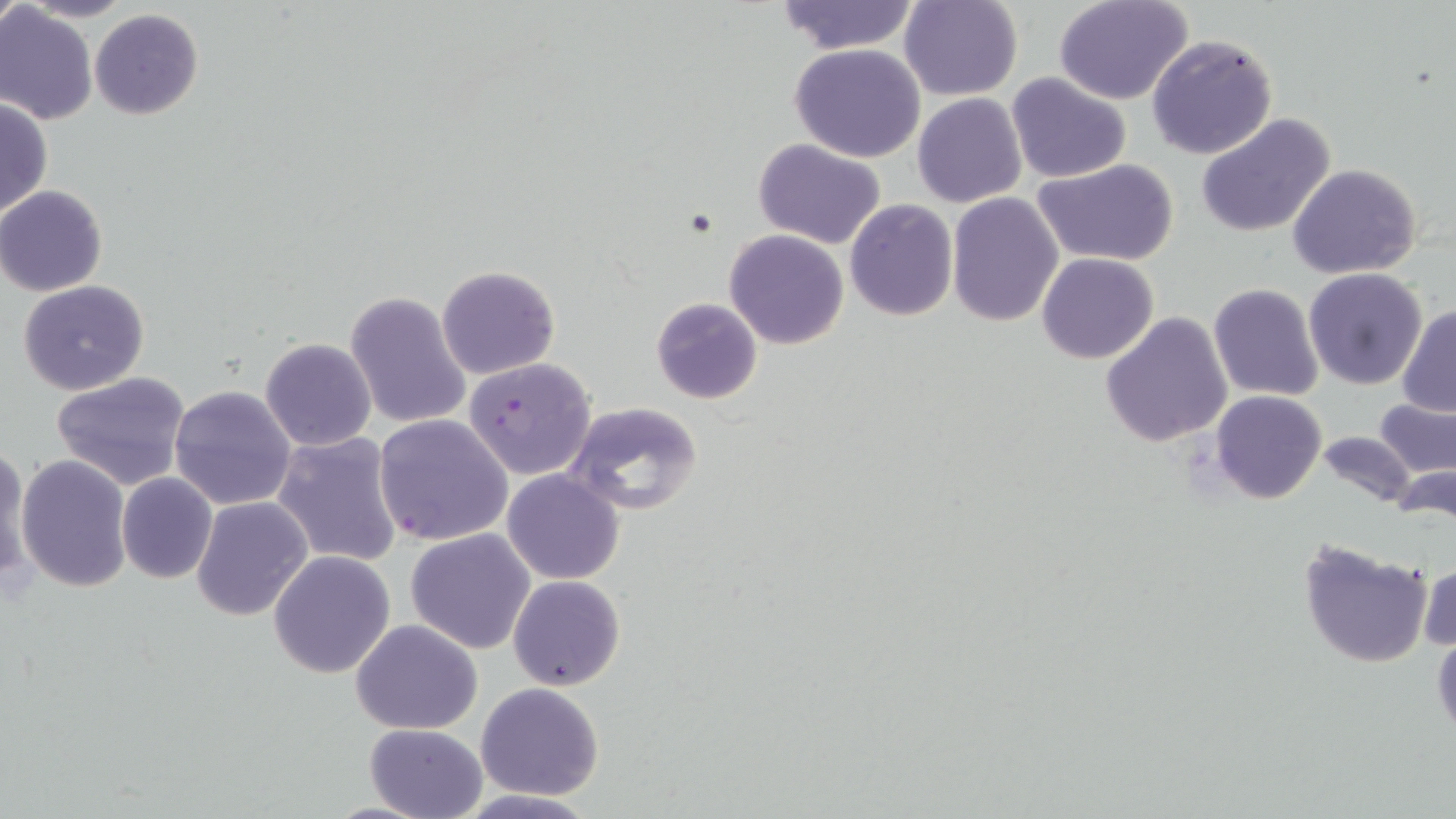
slide_level_diagnosis: Plasmodium falciparum
image_size: 1456×819 pixels
magnification: 1000x
stain: May-Grünwald-Giemsa
plasmodium_falciparum_infected_red_blood_cell_locations: 'approximate bounding boxes as named x1/y1/x2/y2 corners in pixels: (x1=465, y1=357, x2=598, y2=480), (x1=374, y1=413, x2=515, y2=545)'
field_of_view: single
modality: optical microscopy
preparation: thin blood film
uninfected_red_blood_cell_locations: 'approximate bounding boxes as named x1/y1/x2/y2 corners in pixels: (x1=0, y1=0, x2=21, y2=37), (x1=20, y1=0, x2=134, y2=22), (x1=772, y1=0, x2=921, y2=54), (x1=899, y1=0, x2=1022, y2=100), (x1=1053, y1=0, x2=1194, y2=105), (x1=0, y1=5, x2=98, y2=125), (x1=89, y1=9, x2=203, y2=120), (x1=1146, y1=33, x2=1278, y2=158), (x1=789, y1=43, x2=927, y2=163), (x1=1006, y1=73, x2=1131, y2=183), (x1=912, y1=93, x2=1027, y2=208), (x1=0, y1=98, x2=51, y2=220), (x1=1196, y1=113, x2=1338, y2=240), (x1=753, y1=138, x2=887, y2=247), (x1=1034, y1=161, x2=1179, y2=266), (x1=1288, y1=164, x2=1423, y2=280), (x1=0, y1=185, x2=108, y2=296), (x1=946, y1=194, x2=1064, y2=327), (x1=845, y1=199, x2=958, y2=321), (x1=724, y1=228, x2=851, y2=348), (x1=1037, y1=253, x2=1159, y2=365), (x1=436, y1=264, x2=561, y2=380), (x1=370, y1=267, x2=528, y2=401), (x1=1303, y1=268, x2=1430, y2=390), (x1=18, y1=281, x2=149, y2=396), (x1=1208, y1=284, x2=1323, y2=401), (x1=345, y1=290, x2=472, y2=431), (x1=649, y1=296, x2=763, y2=404), (x1=1397, y1=304, x2=1456, y2=417), (x1=1100, y1=312, x2=1233, y2=448), (x1=261, y1=338, x2=377, y2=451), (x1=50, y1=371, x2=191, y2=491), (x1=169, y1=385, x2=296, y2=510), (x1=1209, y1=390, x2=1327, y2=505), (x1=1375, y1=398, x2=1455, y2=478), (x1=566, y1=400, x2=704, y2=515), (x1=1315, y1=431, x2=1419, y2=513), (x1=271, y1=433, x2=403, y2=567), (x1=0, y1=444, x2=32, y2=587), (x1=16, y1=454, x2=132, y2=592), (x1=503, y1=469, x2=624, y2=584), (x1=117, y1=472, x2=218, y2=584), (x1=191, y1=495, x2=313, y2=622), (x1=405, y1=528, x2=536, y2=654), (x1=1297, y1=536, x2=1433, y2=668), (x1=268, y1=551, x2=397, y2=679), (x1=1417, y1=557, x2=1455, y2=655), (x1=507, y1=575, x2=626, y2=690), (x1=351, y1=620, x2=482, y2=734), (x1=1431, y1=629, x2=1456, y2=741), (x1=476, y1=682, x2=605, y2=802), (x1=363, y1=722, x2=488, y2=819)'